Assess the morphology of the red blood cells.
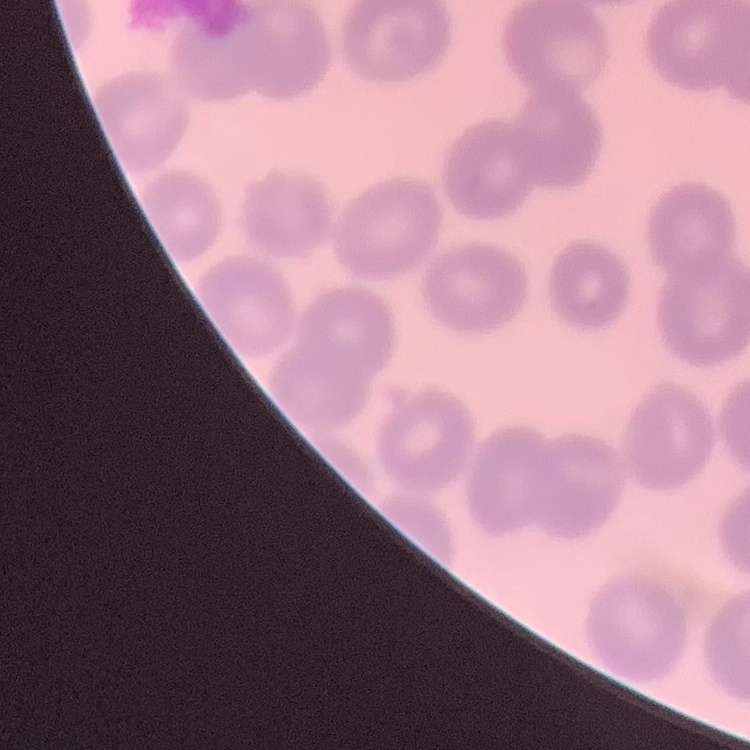
No rouleaux formation.

Thin blood film. Field's or Giemsa stain. One tile cut from a larger photomicrograph.